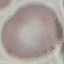
Summary:
  - Malaria status: uninfected
  - Capture: smartphone through the microscope eyepiece
  - Image type: automatically extracted cell patch, resized to 64 × 64 pixels
  - Preparation: thin blood film
  - Stain: Giemsa